Classify this cell by malaria status.
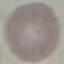
Uninfected.

Summary:
  - Image type: automatically extracted cell patch, resized to 64 × 64 pixels
  - Capture: smartphone camera at the microscope eyepiece
  - Stain: Giemsa
  - Preparation: thin blood smear